Classify this cell by malaria status.
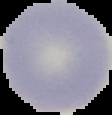
Uninfected.

From a thin blood film. The area outside the segmented cell region is set to black. Image is 112×115 pixels.